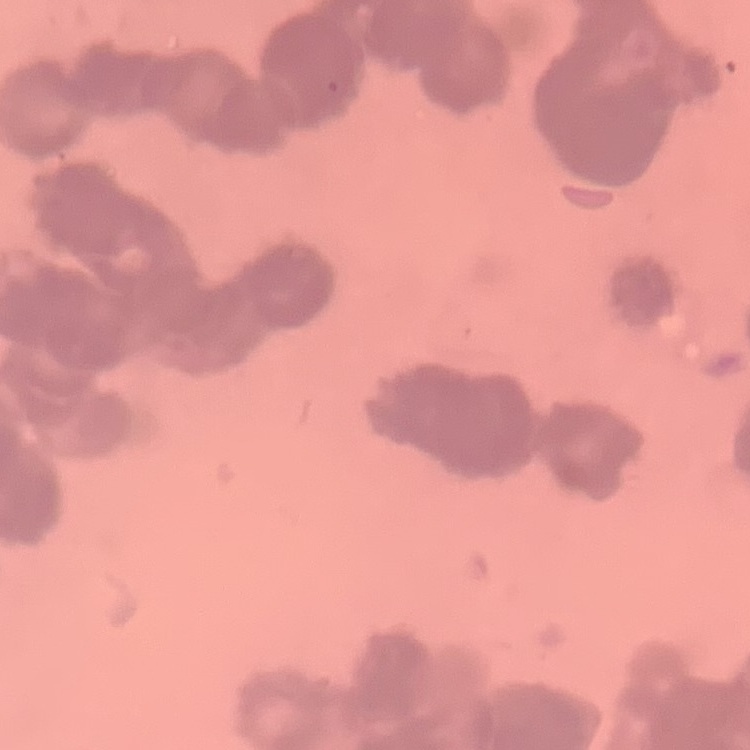

The red blood cells show rouleaux formation. One tile cut from a larger photomicrograph. Thin blood smear. Stained with either Field's or Giemsa.